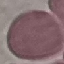
Summary:
  - Result: negative for malaria parasites
  - Stain: Giemsa
  - Preparation: thin blood film
  - Capture: smartphone through the microscope eyepiece
  - Image type: cell patch, automatically extracted from a larger field of view and resized to 64 × 64 pixels